Identify the parasite.
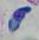
This is Toxoplasma gondii.

modality = micrograph
magnification = 1000x